Assess this cell for malaria.
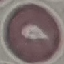

Uninfected.

Giemsa stain. Acquired by smartphone through the microscope eyepiece. Automatically extracted cell patch, resized to 64 × 64 pixels. Thin smear of blood.